Identify the parasite.
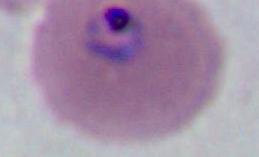

Plasmodium.

Photomicrograph. Captured at either 400x or 1000x magnification.